State the blood parasite species.
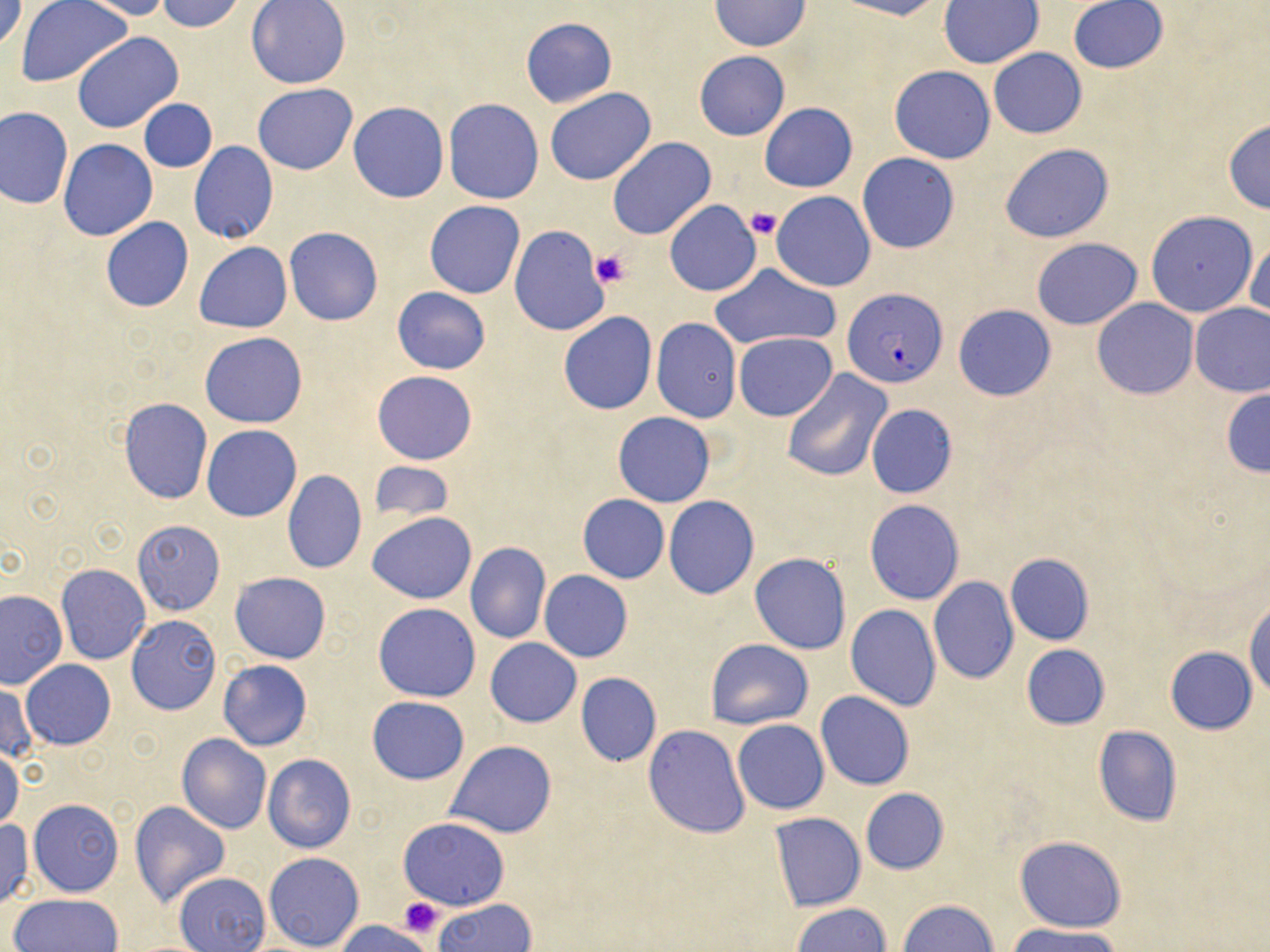
Plasmodium falciparum.

Summary:
  - Coordinate format: approximate bounding boxes as [x1, y1, x2, y2] in pixels
  - Uninfected red blood cell locations: [1, 0, 26, 53], [18, 0, 130, 88], [79, 0, 174, 20], [155, 0, 247, 32], [832, 0, 941, 20], [1068, 0, 1168, 74], [246, 1, 350, 88], [709, 1, 810, 51], [938, 1, 1044, 68], [520, 17, 617, 107], [72, 32, 184, 133], [988, 48, 1086, 138], [694, 51, 789, 140], [889, 66, 995, 163], [253, 84, 358, 174], [544, 88, 656, 186], [443, 98, 545, 204], [140, 99, 217, 172], [760, 102, 857, 191], [349, 103, 449, 203], [0, 106, 72, 209], [1222, 118, 1270, 213], [607, 137, 716, 239], [59, 139, 156, 240], [189, 142, 277, 245], [1000, 143, 1114, 243], [857, 153, 959, 254], [772, 191, 875, 291], [423, 201, 525, 299], [664, 201, 762, 297], [1145, 210, 1258, 318], [100, 217, 194, 313], [509, 225, 610, 337], [284, 227, 384, 325], [1031, 237, 1143, 329], [1246, 237, 1269, 324], [195, 242, 292, 332], [709, 263, 839, 351], [392, 287, 490, 375], [1092, 298, 1198, 399], [1189, 302, 1270, 396], [953, 304, 1056, 401], [558, 311, 658, 415], [650, 317, 742, 423], [200, 331, 308, 428], [733, 332, 836, 421], [373, 369, 477, 465], [781, 369, 893, 482], [1221, 387, 1269, 478], [119, 398, 212, 502], [865, 403, 958, 497], [613, 412, 714, 508], [201, 425, 301, 521], [369, 461, 454, 523], [282, 469, 366, 573], [578, 495, 669, 583], [663, 496, 759, 599], [865, 499, 965, 604], [367, 512, 476, 604], [132, 520, 225, 616], [465, 541, 551, 643], [750, 553, 851, 655], [1005, 553, 1095, 645], [57, 563, 149, 664], [539, 570, 633, 662], [230, 572, 332, 663], [928, 577, 1019, 684], [0, 590, 67, 688], [1245, 596, 1270, 698], [374, 602, 481, 702], [846, 603, 940, 709], [126, 615, 221, 715], [486, 638, 581, 727], [704, 639, 812, 729], [1021, 644, 1111, 730], [1165, 647, 1257, 734], [21, 659, 115, 750], [218, 659, 312, 751], [575, 672, 662, 766], [0, 683, 37, 766], [815, 692, 914, 790], [367, 695, 470, 784], [732, 719, 829, 814], [643, 724, 751, 839], [1092, 726, 1183, 826], [177, 734, 272, 834], [445, 740, 556, 838], [0, 747, 23, 832], [264, 754, 356, 853], [859, 787, 949, 874], [29, 799, 124, 896], [130, 801, 230, 907], [770, 812, 865, 911], [398, 816, 509, 910], [0, 820, 33, 908], [1015, 836, 1125, 932], [263, 852, 364, 952], [175, 872, 270, 952], [8, 894, 126, 951], [434, 898, 536, 952], [899, 898, 999, 952], [791, 902, 892, 952], [335, 919, 437, 952], [1009, 925, 1127, 952]
  - Plasmodium falciparum-infected red blood cell locations: [842, 289, 947, 388]
  - Platelet locations: [746, 207, 782, 241], [592, 249, 627, 288], [400, 898, 443, 937]
  - Field of view: one of a larger specimen
  - Image size: 1270×952 pixels
  - Preparation: thin blood film
  - Stain: May-Grünwald-Giemsa
  - Magnification: 1000x
  - Modality: optical microscopy